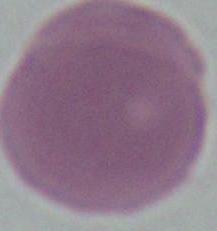

Captured at 1000x magnification. Micrograph. A red blood cell is shown.